Locate every blood parasite and identify its species.
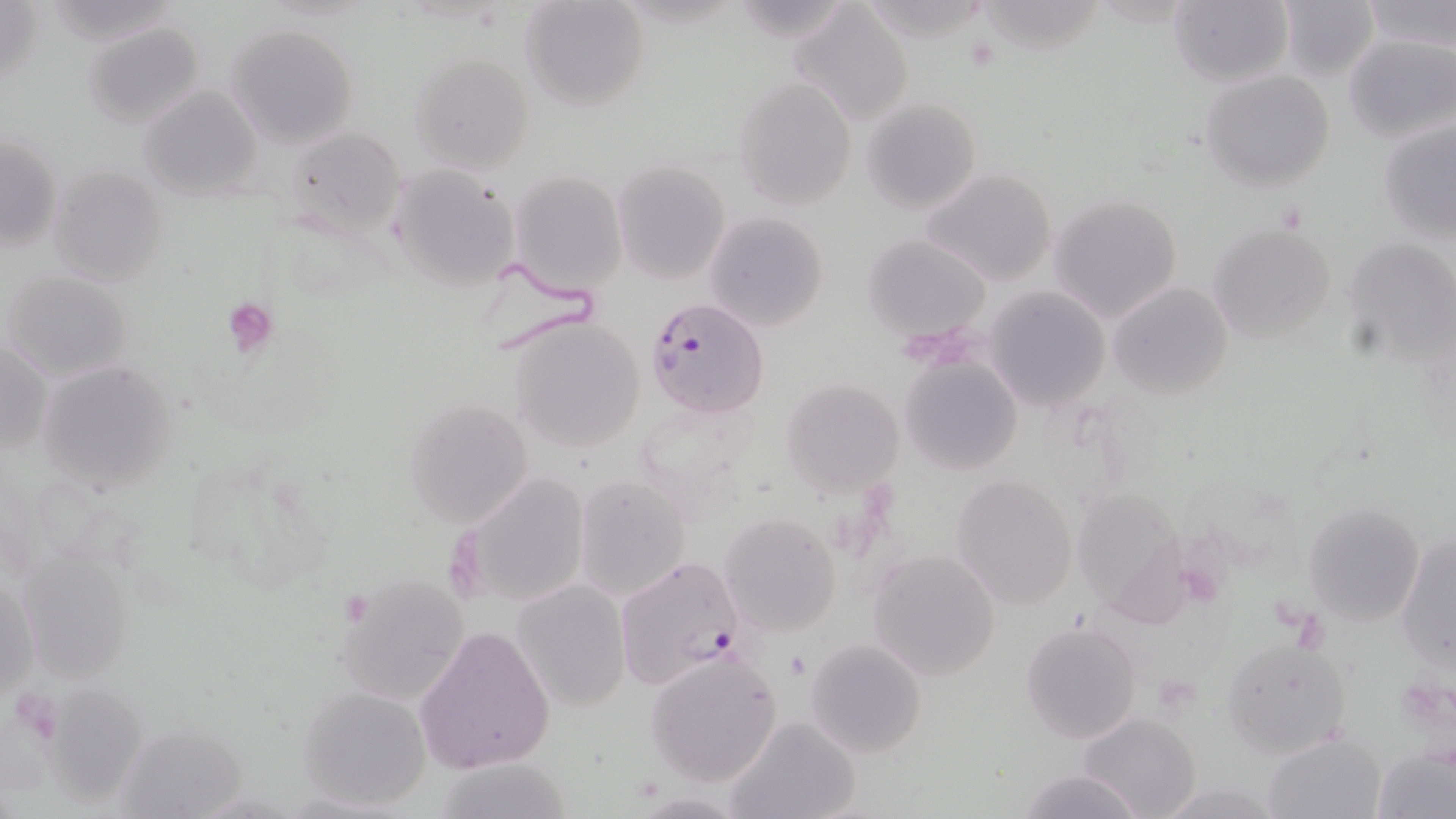
Approximate bounding boxes as (x1,y1)-(x2,y2) corner pairs in pixels.
Plasmodium falciparum-infected red blood cells: (645,298)-(769,419), (615,555)-(744,690).
No Plasmodium ovale, Plasmodium malariae, Plasmodium vivax, Babesia divergens, or Trypanosoma brucei observed.

Summary:
  - Platelet locations: (962,34)-(1003,72), (225,298)-(278,354), (9,688)-(62,741)
  - Uninfected red blood cell locations: (38,0)-(186,47), (520,0)-(649,112), (1167,0)-(1292,88), (1275,0)-(1380,81), (1359,0)-(1455,53), (0,1)-(46,94), (793,3)-(915,124), (80,21)-(207,130), (227,22)-(359,149), (1344,34)-(1455,142), (408,50)-(536,174), (1199,69)-(1335,192), (733,77)-(857,209), (138,85)-(261,200), (861,97)-(982,216), (1378,117)-(1456,243), (283,126)-(407,240), (0,133)-(62,252), (613,159)-(730,284), (48,162)-(171,287), (390,163)-(521,294), (920,167)-(1060,288), (508,170)-(629,298), (1049,195)-(1183,323), (704,211)-(831,333), (1209,220)-(1338,344), (863,233)-(991,343), (1345,235)-(1456,364), (2,269)-(135,383), (1107,281)-(1234,401), (983,287)-(1109,410), (505,314)-(646,452), (1,339)-(48,456), (900,356)-(1022,475), (35,360)-(180,497), (781,378)-(904,496), (401,398)-(533,527), (634,398)-(760,507), (451,472)-(590,611), (574,474)-(690,600), (949,474)-(1078,610), (1072,488)-(1194,619), (1304,500)-(1425,626), (720,512)-(841,637), (1395,532)-(1455,670), (17,548)-(141,686), (868,549)-(1001,681), (336,573)-(468,704), (1,574)-(40,701), (511,580)-(631,711), (1021,620)-(1141,745), (412,625)-(556,774), (1221,637)-(1352,758), (805,638)-(927,758), (643,650)-(784,786), (297,684)-(433,811), (43,689)-(150,804), (1080,710)-(1203,819), (722,716)-(861,819), (111,719)-(251,819), (1263,732)-(1387,818), (1374,746)-(1455,819), (430,757)-(579,818), (1015,768)-(1141,819), (1152,779)-(1288,817)
  - Slide-level diagnosis: Plasmodium falciparum
  - Field of view: one of a larger specimen
  - Preparation: thin blood smear
  - Magnification: 1000x
  - Modality: light microscopy
  - Stain: May-Grünwald-Giemsa
  - Image size: 1456×819 pixels